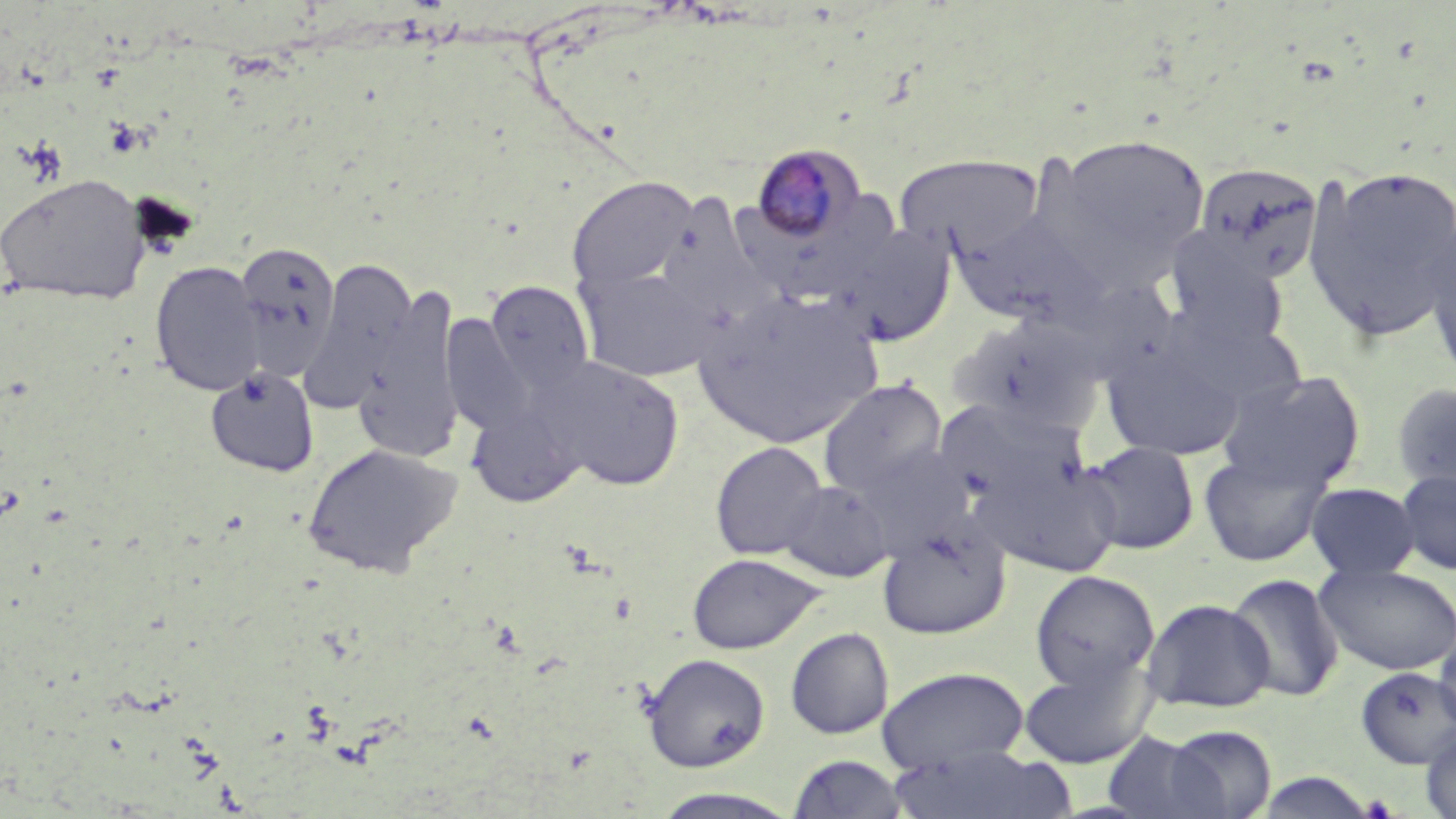 Approximate bounding boxes as (x1, y1, x2, y2) in pixels. Plasmodium malariae-infected red blood cell locations: (749, 142, 867, 246). Uninfected red blood cell locations: (1037, 132, 1212, 289), (893, 152, 1045, 259), (1193, 164, 1325, 283), (1301, 165, 1456, 342), (0, 173, 152, 305), (567, 176, 698, 295), (666, 191, 782, 325), (949, 210, 1106, 327), (1419, 216, 1456, 380), (833, 224, 957, 347), (1165, 236, 1288, 347), (233, 240, 342, 378), (299, 257, 417, 415), (150, 261, 264, 396), (575, 263, 722, 382), (1050, 275, 1181, 388), (484, 280, 596, 396), (355, 282, 463, 462), (692, 288, 883, 448), (442, 314, 537, 437), (949, 314, 1104, 437), (1101, 338, 1245, 461), (537, 356, 687, 491), (204, 366, 320, 479), (1216, 369, 1367, 493), (818, 378, 949, 500), (1391, 382, 1456, 495), (936, 400, 1090, 514), (467, 401, 585, 508), (710, 440, 828, 560), (1081, 441, 1200, 554), (302, 442, 463, 578), (975, 450, 1124, 579), (1198, 450, 1332, 566), (1395, 468, 1456, 576), (778, 481, 893, 581), (1305, 482, 1421, 580), (877, 518, 1011, 640), (686, 552, 824, 655), (1314, 563, 1456, 676), (1029, 569, 1160, 693), (1226, 574, 1344, 702), (1141, 598, 1276, 713), (1432, 626, 1456, 739), (785, 627, 893, 739), (641, 652, 770, 772), (1018, 655, 1155, 769), (876, 666, 1030, 774), (1356, 666, 1456, 769), (1162, 724, 1278, 818), (1420, 726, 1456, 819), (1101, 731, 1223, 818), (885, 743, 1077, 819), (786, 753, 912, 818), (1252, 771, 1381, 818), (647, 788, 805, 819). Slide-level diagnosis: Plasmodium malariae. Optical microscopy. Image is 1456×819 pixels. One field of a larger specimen. 1000x magnification. May-Grünwald-Giemsa stain. Thin blood smear.